Report the malaria status of this cell.
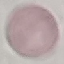
It is uninfected.

Photographed with a smartphone camera at the microscope eyepiece. Automatically extracted cell patch, resized to 64 × 64 pixels. Giemsa stain. Thin blood film.